Assess this cell for malaria.
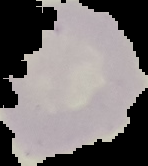

Parasitized.

image size = 148×166 pixels
preparation = thin blood film
image type = segmented cell region on a black background